Assess the morphology of the red blood cells.
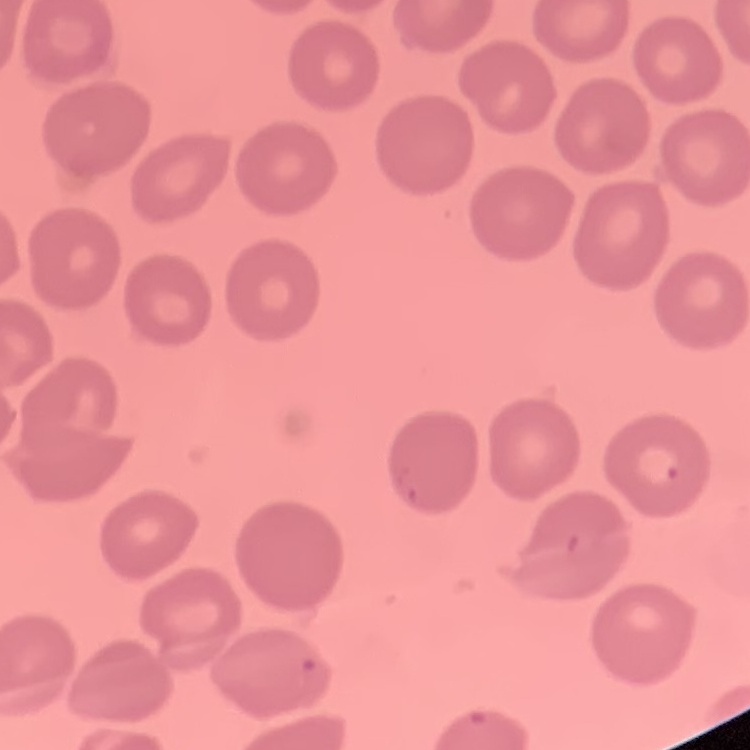

They show no rouleaux formation.

Summary:
  - Image type: square crop of a larger photomicrograph
  - Preparation: thin blood smear
  - Stain: Field's or Giemsa